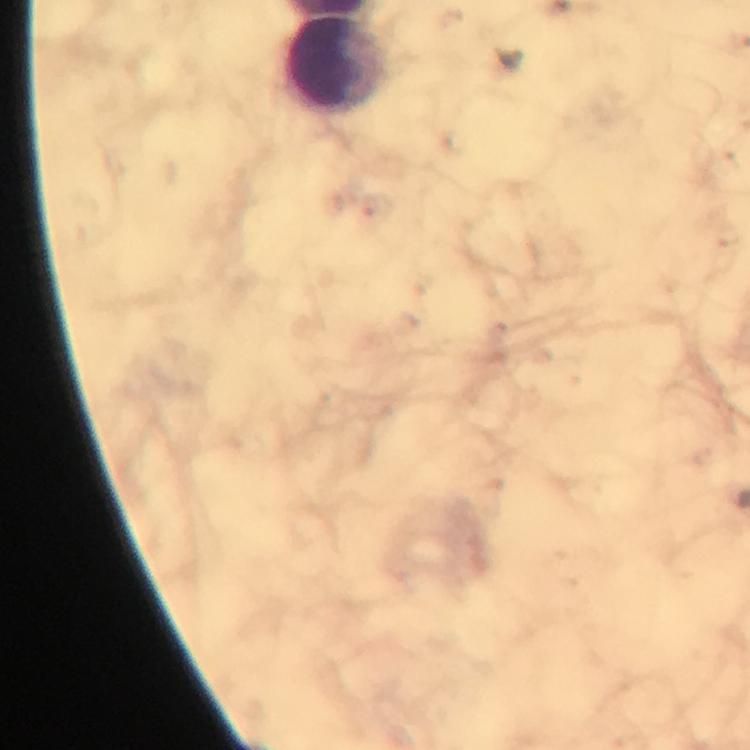
Approximate centers as (x, y) in pixels.
Summary:
  - Leukocyte locations: (335, 65)
  - Cropped from: one field of view
  - Stain: Giemsa
  - Immersion oil: applied
  - Image size: 750×750 pixels
  - Context: from a malaria diagnostic workup
  - Plasmodium parasites: none seen
  - Magnification: 100x
  - Preparation: thick blood film
  - Capture: smartphone mounted on the microscope